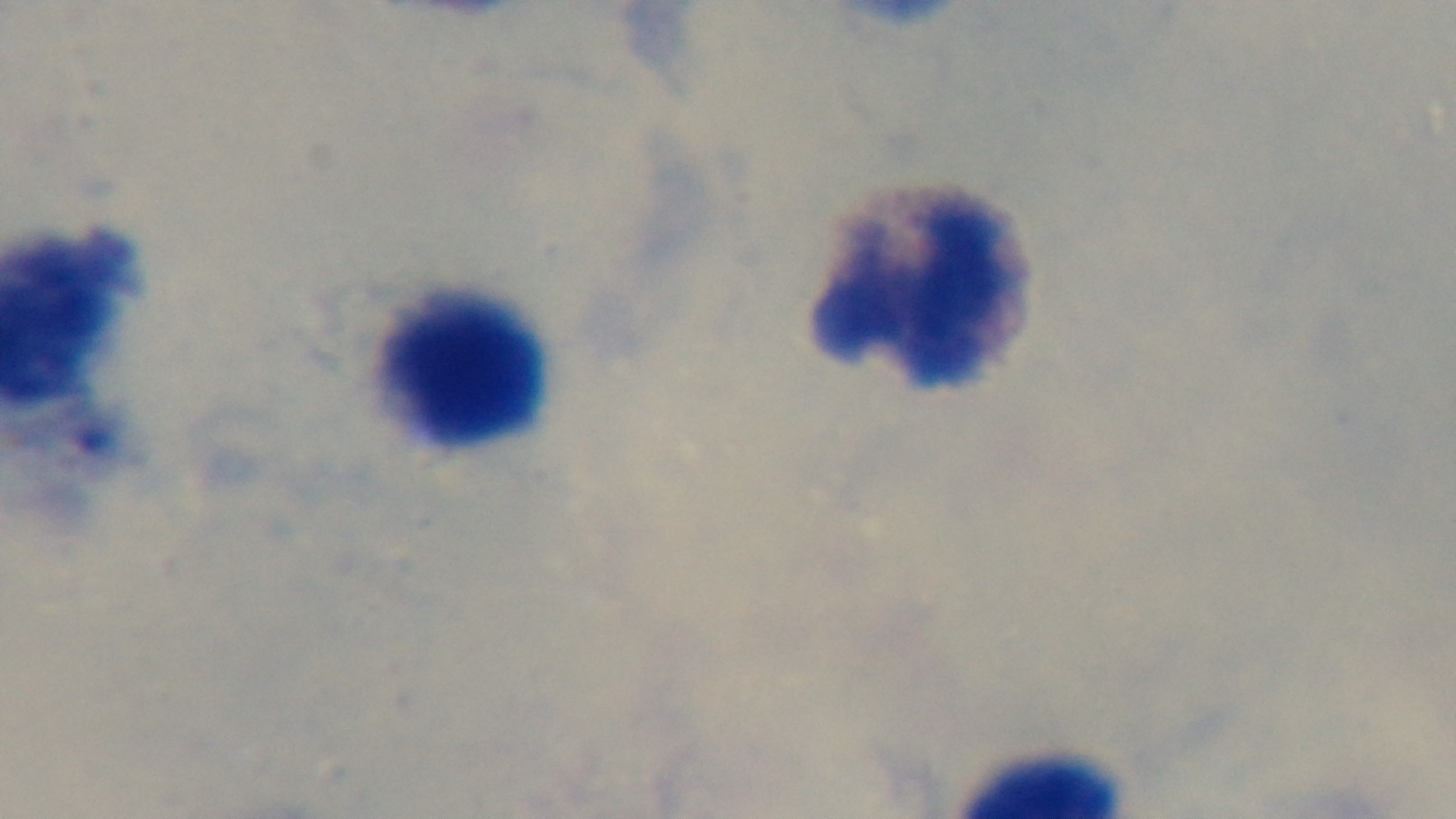
preparation = thick
objective = 100x oil immersion
modality = light microscopy
capture = mounted 4K digital camera
stain = Giemsa
malaria status = uninfected
field of view = single